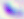

Toxoplasma gondii is seen. Micrograph. 400x magnification.